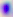

magnification = 400x
modality = micrograph
identification = Toxoplasma gondii